Give the preparation type.
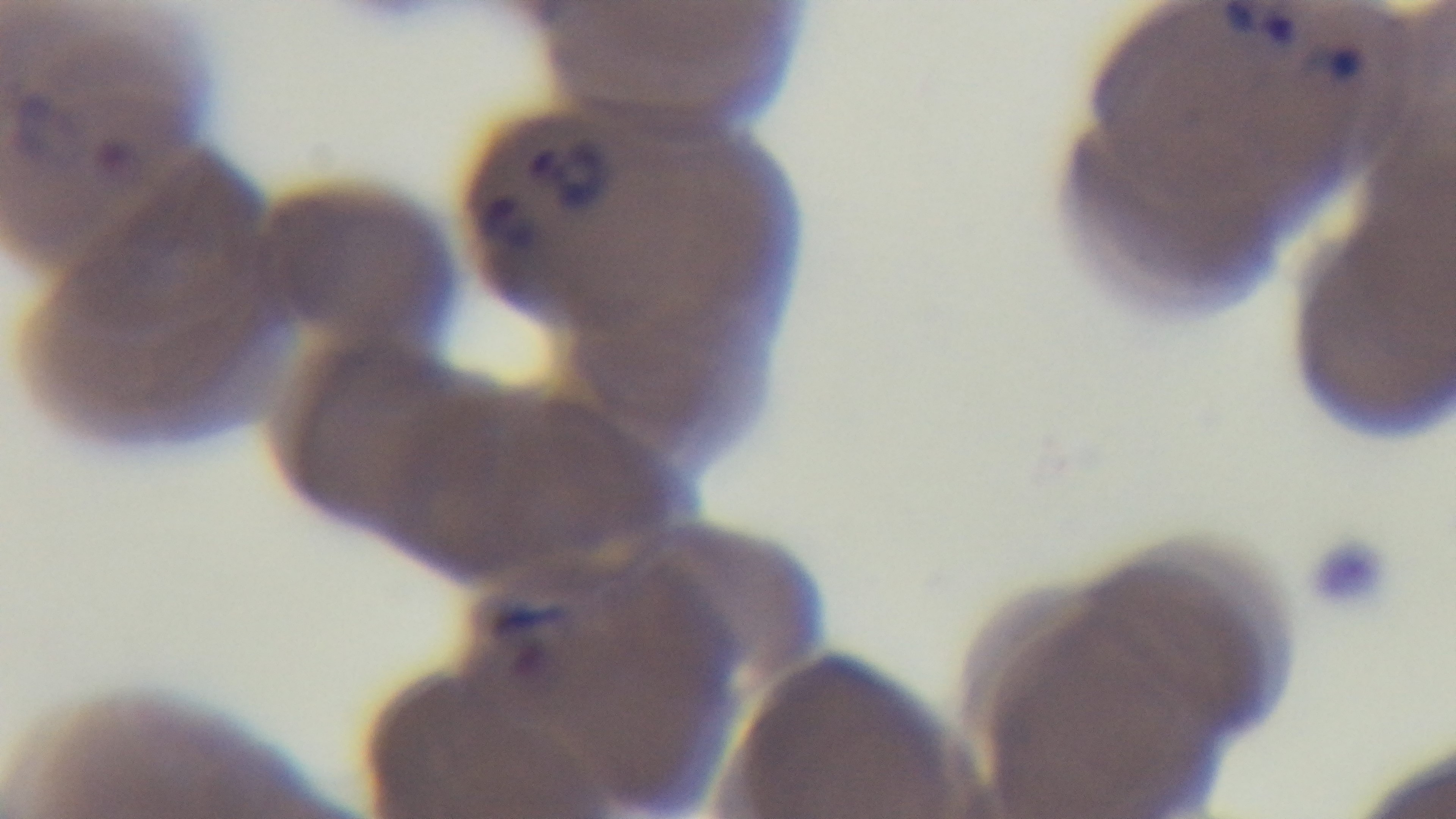
It is a thin blood film.

objective = 100x oil immersion
stain = Giemsa
capture = mounted 4K digital camera
field of view = one from the slide
malaria status = infected
modality = light microscopy